Outline platelets.
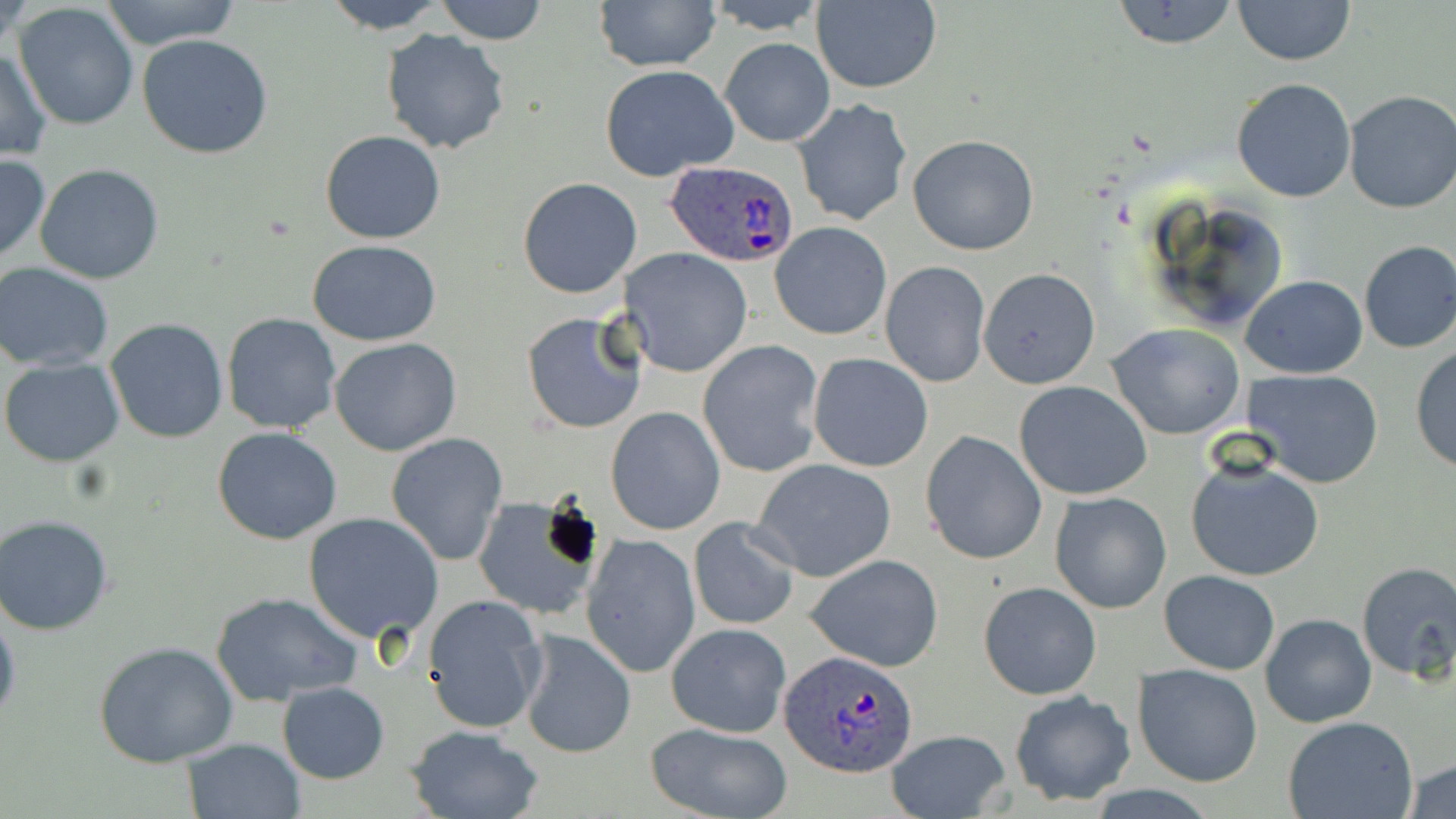
Approximate bounding boxes as (x1,y1)-(x2,y2) corner pairs in pixels.
Platelets: (536,501)-(605,576).

Summary:
  - Plasmodium ovale-infected red blood cell locations: (664,160)-(799,268), (780,649)-(918,776)
  - Uninfected red blood cell locations: (100,0)-(242,49), (321,0)-(449,34), (437,0)-(546,44), (592,0)-(720,71), (700,0)-(829,33), (1110,0)-(1242,50), (1233,0)-(1355,66), (811,1)-(941,94), (14,3)-(139,131), (380,28)-(509,153), (137,35)-(272,159), (719,36)-(833,145), (1,45)-(52,161), (599,63)-(739,181), (1231,78)-(1358,203), (1342,91)-(1456,213), (793,98)-(912,228), (319,129)-(447,244), (907,134)-(1040,257), (0,153)-(49,266), (34,163)-(164,284), (517,177)-(640,299), (770,222)-(892,339), (307,239)-(441,346), (1357,240)-(1456,354), (622,248)-(753,379), (880,261)-(990,387), (0,262)-(115,371), (978,267)-(1100,389), (1241,274)-(1368,380), (521,311)-(642,435), (222,312)-(343,435), (104,317)-(231,444), (1108,323)-(1245,439), (330,338)-(462,456), (698,341)-(825,476), (1410,345)-(1456,473), (808,353)-(934,473), (1,358)-(124,465), (1246,370)-(1386,490), (1014,380)-(1152,500), (606,406)-(725,534), (212,427)-(342,545), (921,430)-(1048,566), (385,433)-(507,565), (1186,454)-(1324,582), (751,458)-(898,581), (1048,492)-(1172,614), (472,495)-(605,622), (303,513)-(445,643), (0,515)-(115,635), (689,519)-(799,631), (581,534)-(700,679), (805,553)-(944,672), (1354,561)-(1456,685), (1158,570)-(1279,675), (977,581)-(1102,701), (210,592)-(363,705), (421,594)-(546,735), (0,604)-(20,733), (1260,612)-(1377,729), (667,621)-(792,738), (515,628)-(636,759), (93,640)-(239,767), (1132,663)-(1263,787), (279,682)-(389,784), (1008,690)-(1135,804), (1282,716)-(1418,819), (641,722)-(795,819), (404,724)-(546,818), (883,728)-(1015,817), (181,737)-(306,818), (1403,759)-(1456,819)
  - Slide-level diagnosis: Plasmodium ovale
  - Stain: May-Grünwald-Giemsa
  - Magnification: 1000x
  - Image size: 1456×819 pixels
  - Preparation: thin blood smear
  - Modality: light microscopy
  - Field of view: single